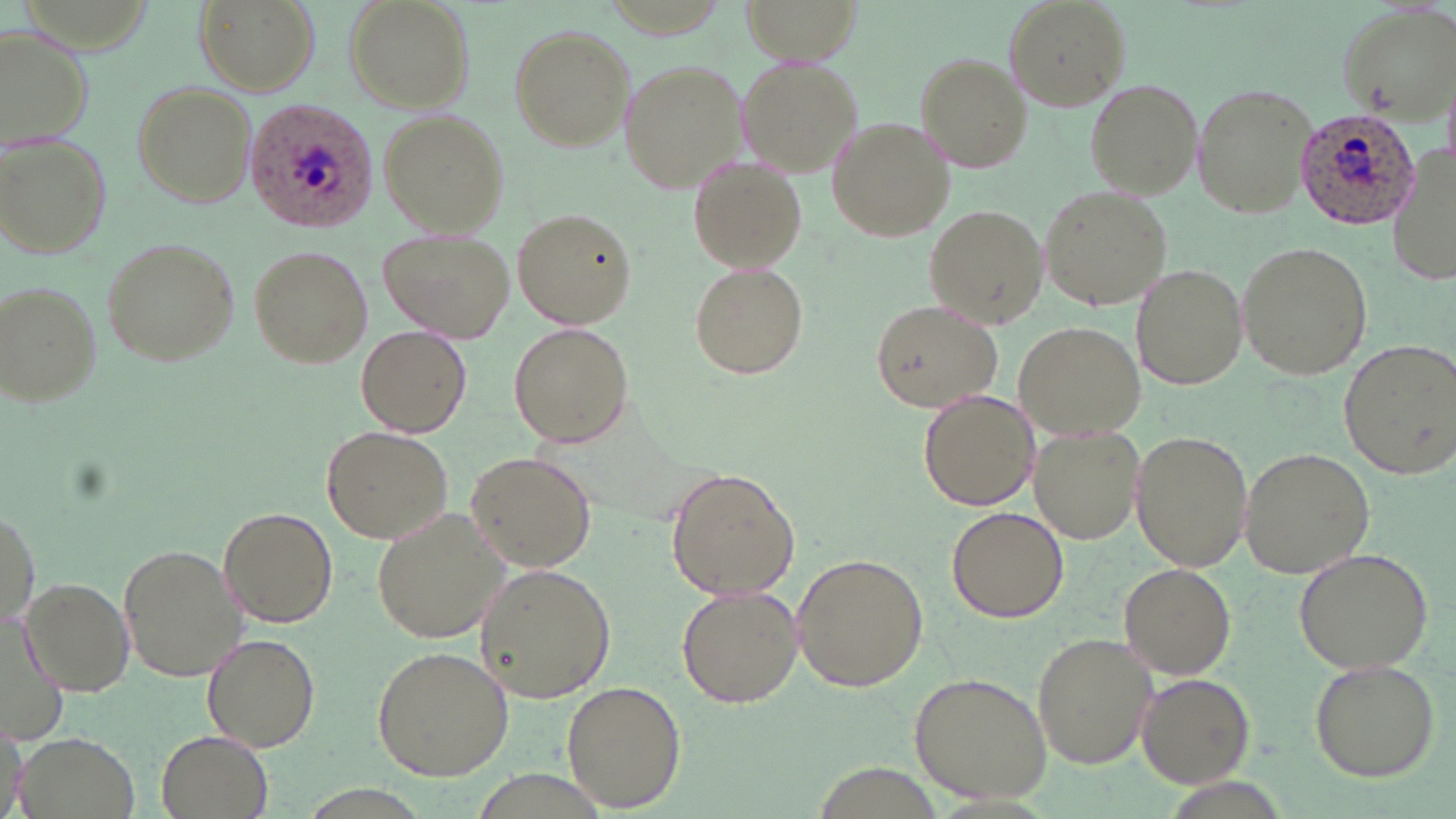

Approximate bounding boxes as named x1/y1/x2/y2 corners in pixels. Plasmodium ovale-infected red blood cell locations: (x1=245, y1=100, x2=378, y2=230), (x1=1294, y1=106, x2=1421, y2=231). Uninfected red blood cell locations: (x1=196, y1=0, x2=318, y2=96), (x1=342, y1=0, x2=473, y2=113), (x1=737, y1=0, x2=863, y2=65), (x1=1005, y1=1, x2=1128, y2=111), (x1=1338, y1=2, x2=1456, y2=120), (x1=0, y1=24, x2=92, y2=145), (x1=508, y1=25, x2=634, y2=152), (x1=913, y1=53, x2=1030, y2=173), (x1=737, y1=55, x2=863, y2=176), (x1=617, y1=57, x2=748, y2=193), (x1=128, y1=79, x2=256, y2=209), (x1=1086, y1=79, x2=1205, y2=199), (x1=1191, y1=82, x2=1318, y2=217), (x1=379, y1=111, x2=511, y2=237), (x1=827, y1=118, x2=954, y2=244), (x1=0, y1=134, x2=111, y2=261), (x1=1389, y1=145, x2=1456, y2=294), (x1=688, y1=154, x2=807, y2=273), (x1=1039, y1=182, x2=1172, y2=314), (x1=925, y1=206, x2=1046, y2=327), (x1=513, y1=208, x2=636, y2=330), (x1=381, y1=227, x2=518, y2=341), (x1=100, y1=235, x2=240, y2=367), (x1=1236, y1=240, x2=1372, y2=380), (x1=247, y1=244, x2=372, y2=368), (x1=688, y1=260, x2=811, y2=380), (x1=1132, y1=262, x2=1248, y2=390), (x1=1, y1=280, x2=103, y2=407), (x1=869, y1=298, x2=1003, y2=413), (x1=1013, y1=322, x2=1144, y2=440), (x1=507, y1=323, x2=635, y2=447), (x1=356, y1=325, x2=471, y2=437), (x1=1338, y1=339, x2=1454, y2=477), (x1=919, y1=388, x2=1042, y2=511), (x1=322, y1=426, x2=453, y2=542), (x1=1028, y1=426, x2=1144, y2=545), (x1=1131, y1=430, x2=1251, y2=573), (x1=1237, y1=446, x2=1373, y2=579), (x1=465, y1=451, x2=597, y2=572), (x1=664, y1=467, x2=800, y2=602), (x1=2, y1=501, x2=39, y2=631), (x1=946, y1=505, x2=1069, y2=623), (x1=217, y1=506, x2=339, y2=625), (x1=372, y1=506, x2=514, y2=646), (x1=118, y1=541, x2=250, y2=684), (x1=1293, y1=546, x2=1434, y2=675), (x1=791, y1=552, x2=930, y2=692), (x1=1118, y1=562, x2=1237, y2=678), (x1=474, y1=563, x2=615, y2=701), (x1=21, y1=577, x2=135, y2=694), (x1=675, y1=585, x2=802, y2=707), (x1=0, y1=614, x2=71, y2=749), (x1=1032, y1=631, x2=1156, y2=768), (x1=202, y1=633, x2=320, y2=752), (x1=371, y1=646, x2=514, y2=779), (x1=1308, y1=657, x2=1440, y2=782), (x1=909, y1=671, x2=1051, y2=804), (x1=1135, y1=671, x2=1254, y2=786), (x1=560, y1=680, x2=686, y2=811), (x1=0, y1=722, x2=28, y2=816), (x1=155, y1=729, x2=274, y2=819), (x1=16, y1=733, x2=139, y2=819). Slide-level diagnosis: Plasmodium ovale. Optical microscopy. Thin blood film. Captured at 1000x magnification. May-Grünwald-Giemsa-stained preparation. Image is 1456×819 pixels. Single field of view.